Name the cell type shown.
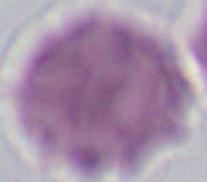

An erythrocyte.

Summary:
  - Modality: micrograph
  - Magnification: 1000x